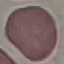

Summary:
  - Malaria status: uninfected
  - Preparation: thin blood film
  - Capture: smartphone through the microscope eyepiece
  - Image type: cell patch, automatically extracted from a larger field of view and resized to 64 × 64 pixels
  - Stain: Giemsa